State which cell type is depicted.
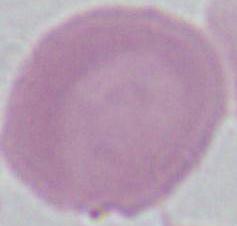

An erythrocyte.

modality = micrograph
magnification = 1000x